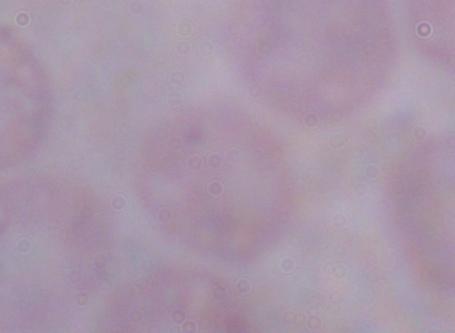
Summary:
  - Magnification: 1000x
  - Identification: trypanosome
  - Modality: photomicrograph